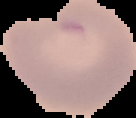

image size = 136×118 pixels
result = no Plasmodium parasites detected
preparation = thin blood smear
image type = segmented cell region with the area outside set to black